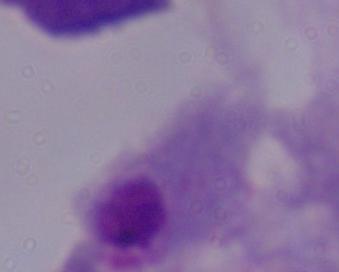
Photomicrograph. A trichomonad is shown. Captured at 1000x magnification.